Give the position of each P. falciparum parasite with its life-cycle stage, each leukocyte, and any debris.
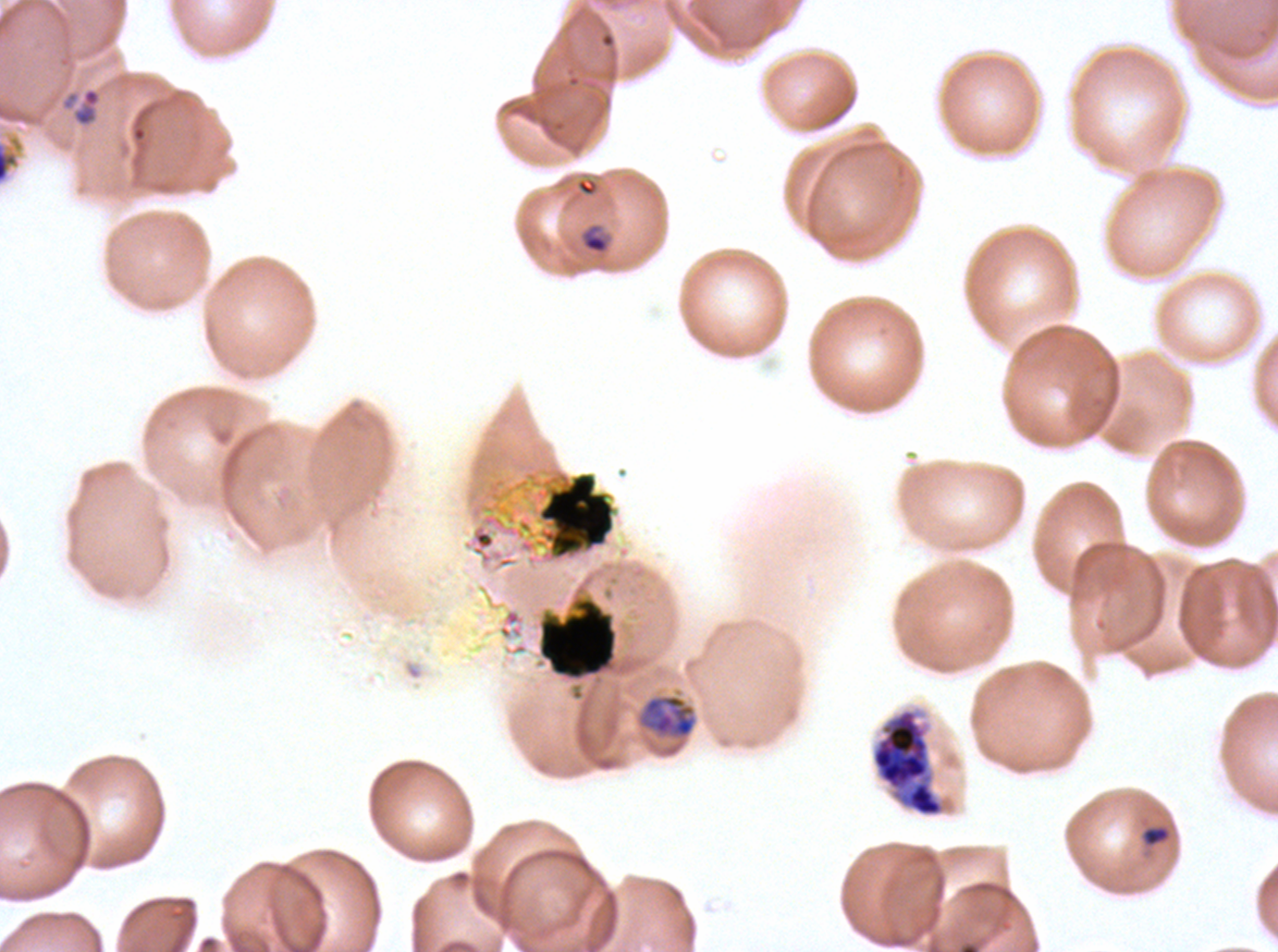

Approximate bounding rectangles given as corner coordinates in pixels from the top-left.
Rings: (x1=60, y1=86, x2=103, y2=128).
Late-ring/early-trophozoite forms: (x1=0, y1=128, x2=26, y2=187), (x1=580, y1=223, x2=610, y2=255).
Late trophozoites: (x1=639, y1=693, x2=696, y2=738).
Late schizonts: (x1=871, y1=708, x2=944, y2=817).
Debris: (x1=536, y1=471, x2=616, y2=560), (x1=536, y1=596, x2=619, y2=681), (x1=1140, y1=824, x2=1172, y2=848).
No mid trophozoites, early schizonts, segmenters, gametocytes, or leukocytes observed.

{
  "preparation": "thin blood film",
  "image_size": "1278×952 pixels",
  "life_cycle_stages_observed": "ring, late-ring/early-trophozoite, late trophozoite, late schizont",
  "stain": "Giemsa",
  "field_of_view": "sub-image separated from a larger composite",
  "specimen": "ex-vivo P. falciparum culture from a patient in The Gambia, grown for 24 to 48 hours"
}